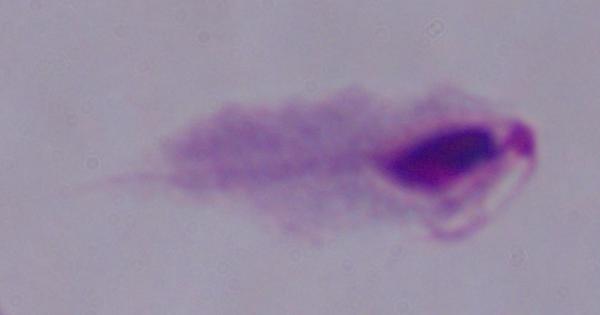
{
  "identification": "trichomonad",
  "magnification": "1000x",
  "modality": "photomicrograph"
}